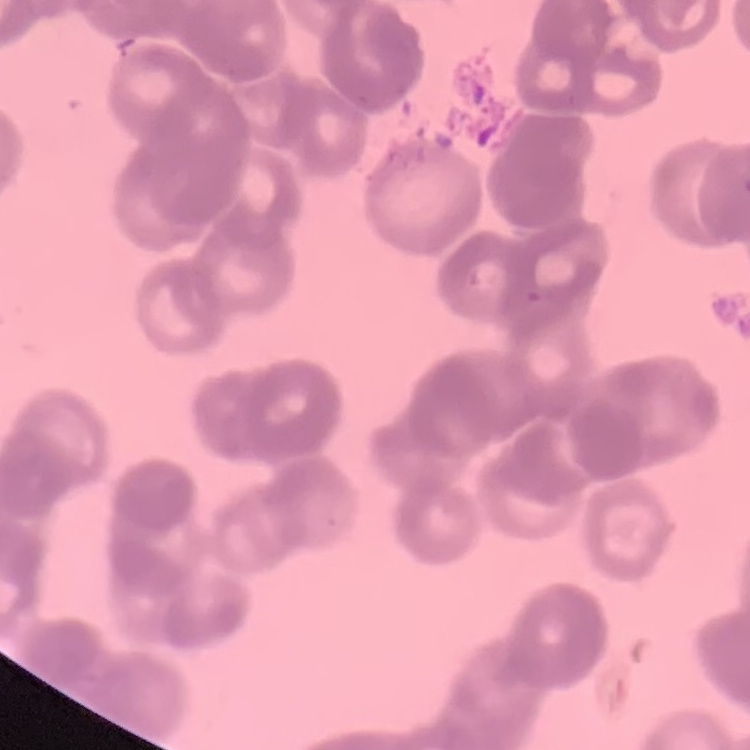
erythrocyte morphology = rouleaux formation
image type = square crop of a larger photomicrograph
stain = Field's or Giemsa
preparation = thin peripheral smear